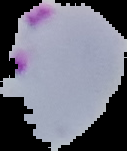

result = Plasmodium parasites detected
image type = segmented cell region on a black background
image size = 127×151 pixels
preparation = thin blood film